Outline each P. falciparum parasite and classify it by life-cycle stage.
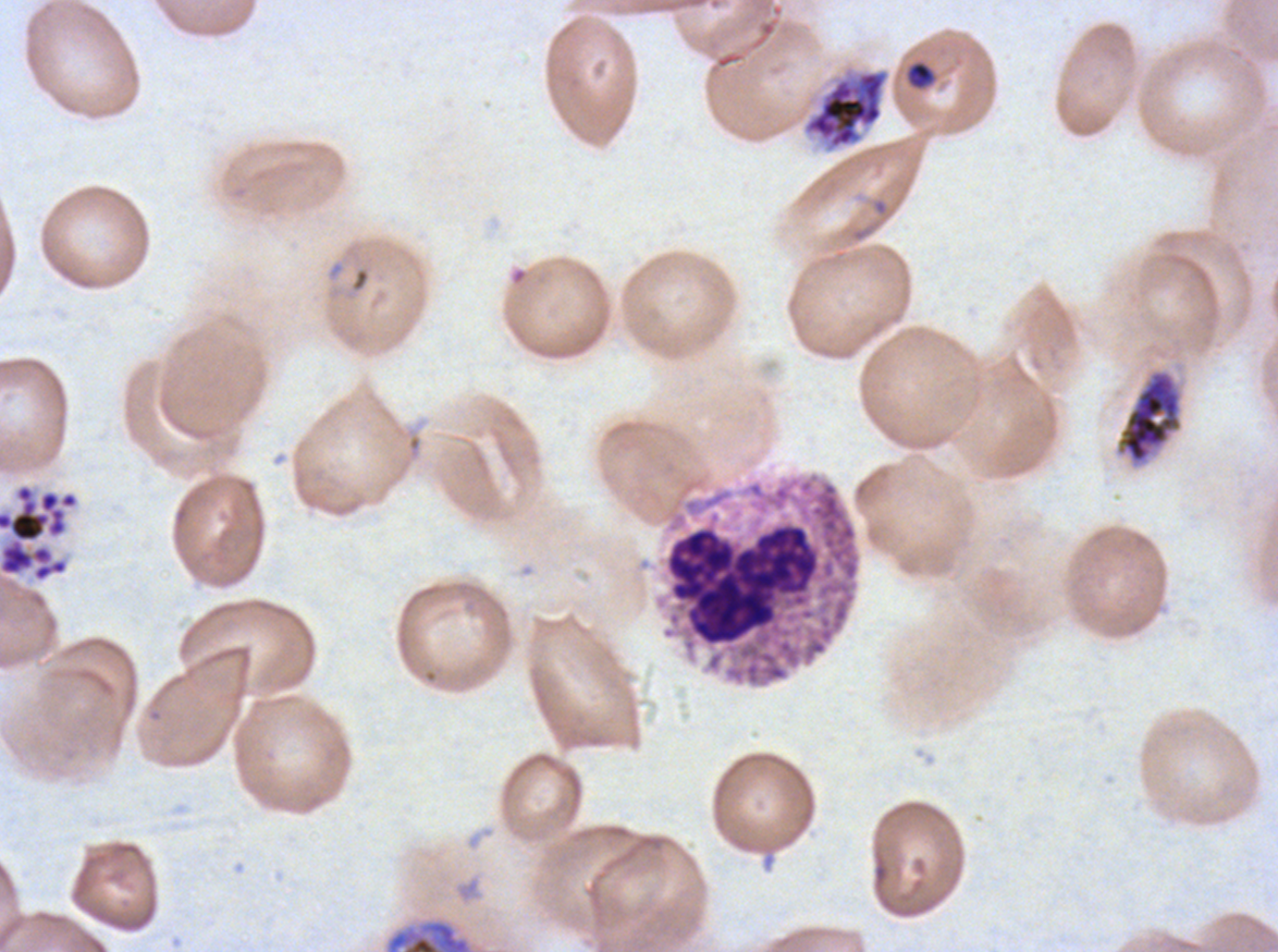
Approximate bounding boxes as (x1, y1, x2, y2) in pixels.
Rings: (348, 265, 372, 295).
Late-ring/early-trophozoite forms: (906, 61, 934, 89).
Early schizonts: (386, 920, 471, 951).
Late schizonts: (1114, 368, 1184, 468).
Segmenters: (805, 71, 886, 148), (0, 483, 79, 582).
No mid trophozoites, late trophozoites, or gametocytes observed.

leukocyte locations = (666, 523, 819, 646)
field of view = one sub-image of a larger composite
image size = 1278×952 pixels
life-cycle stages observed = ring, late-ring/early-trophozoite, early schizont, late schizont, segmenter
preparation = thin blood film
specimen = P. falciparum from a patient in The Gambia, cultured ex vivo for 24 to 48 hours
stain = Giemsa